Locate and identify every blood parasite.
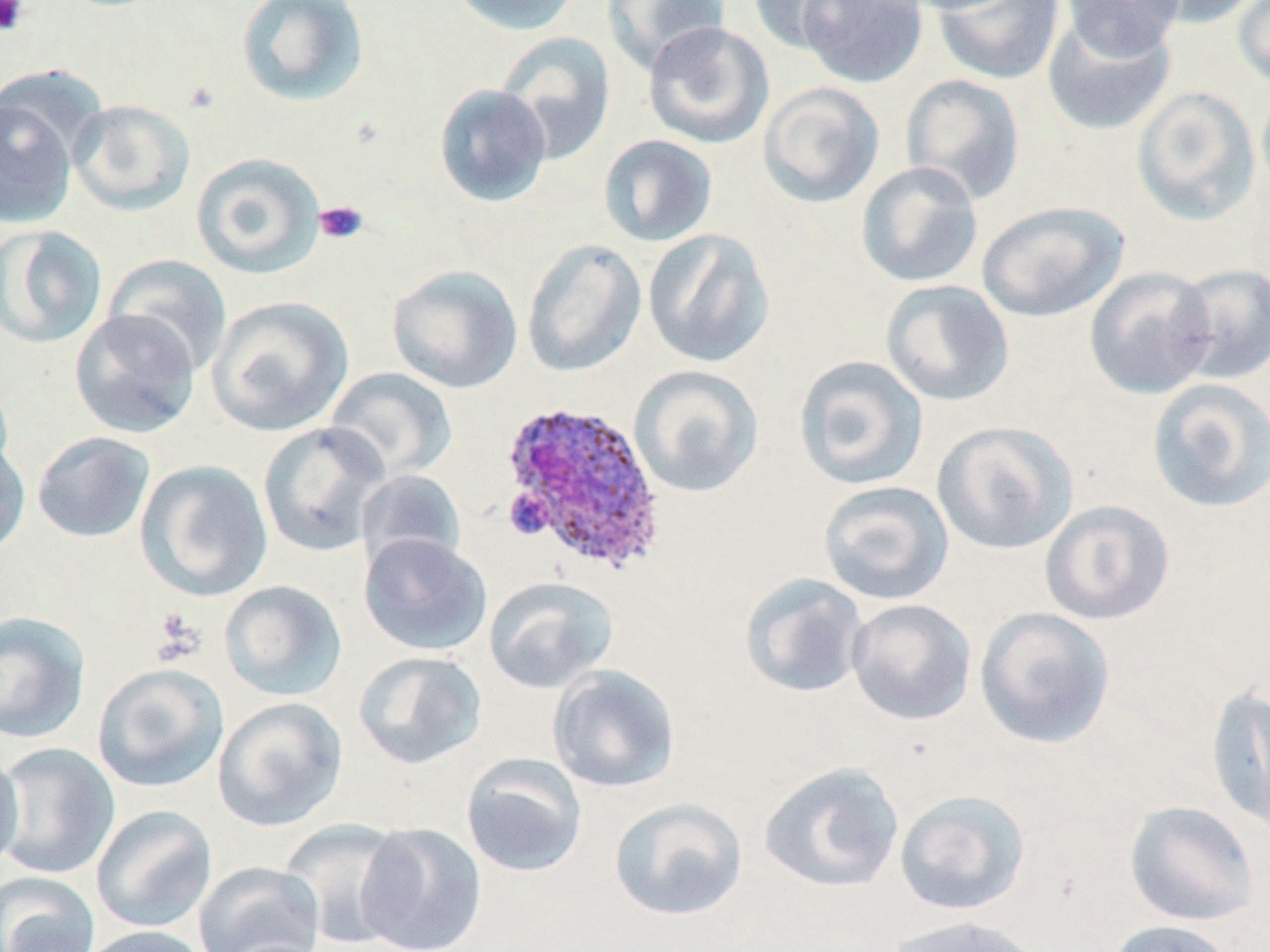

Approximate bounding boxes as named x1/y1/x2/y2 corners in pixels.
Plasmodium ovale-infected red blood cells: (x1=498, y1=398, x2=668, y2=575).
No Plasmodium falciparum, Plasmodium malariae, Plasmodium vivax, Babesia divergens, or Trypanosoma brucei observed.

Summary:
  - Uninfected red blood cell locations: (x1=235, y1=0, x2=370, y2=108), (x1=446, y1=0, x2=583, y2=35), (x1=600, y1=0, x2=731, y2=76), (x1=746, y1=0, x2=868, y2=55), (x1=798, y1=0, x2=929, y2=88), (x1=1062, y1=0, x2=1185, y2=59), (x1=1135, y1=0, x2=1263, y2=29), (x1=1232, y1=0, x2=1270, y2=94), (x1=933, y1=1, x2=1065, y2=85), (x1=1041, y1=9, x2=1176, y2=136), (x1=642, y1=21, x2=775, y2=150), (x1=495, y1=31, x2=616, y2=165), (x1=900, y1=74, x2=1025, y2=205), (x1=757, y1=82, x2=885, y2=208), (x1=1256, y1=83, x2=1270, y2=203), (x1=433, y1=84, x2=553, y2=207), (x1=1131, y1=86, x2=1260, y2=226), (x1=0, y1=91, x2=80, y2=230), (x1=67, y1=99, x2=196, y2=216), (x1=597, y1=134, x2=718, y2=248), (x1=190, y1=152, x2=326, y2=279), (x1=855, y1=161, x2=984, y2=287), (x1=976, y1=200, x2=1128, y2=323), (x1=0, y1=225, x2=108, y2=349), (x1=642, y1=228, x2=775, y2=369), (x1=521, y1=237, x2=647, y2=378), (x1=103, y1=254, x2=232, y2=376), (x1=1172, y1=263, x2=1269, y2=384), (x1=387, y1=264, x2=523, y2=394), (x1=1084, y1=266, x2=1217, y2=400), (x1=880, y1=280, x2=1015, y2=407), (x1=206, y1=295, x2=354, y2=437), (x1=68, y1=309, x2=201, y2=439), (x1=793, y1=355, x2=929, y2=490), (x1=629, y1=365, x2=764, y2=498), (x1=324, y1=367, x2=457, y2=482), (x1=1146, y1=378, x2=1270, y2=513), (x1=932, y1=420, x2=1079, y2=555), (x1=257, y1=421, x2=391, y2=558), (x1=32, y1=431, x2=156, y2=542), (x1=0, y1=436, x2=31, y2=561), (x1=134, y1=459, x2=274, y2=602), (x1=356, y1=469, x2=466, y2=574), (x1=817, y1=480, x2=954, y2=605), (x1=1039, y1=499, x2=1175, y2=625), (x1=358, y1=533, x2=493, y2=656), (x1=739, y1=573, x2=870, y2=699), (x1=483, y1=576, x2=618, y2=694), (x1=219, y1=580, x2=347, y2=702), (x1=846, y1=598, x2=977, y2=726), (x1=974, y1=606, x2=1117, y2=750), (x1=0, y1=611, x2=91, y2=744), (x1=353, y1=650, x2=487, y2=770), (x1=92, y1=662, x2=229, y2=793), (x1=547, y1=664, x2=682, y2=794), (x1=1205, y1=682, x2=1270, y2=830), (x1=212, y1=697, x2=348, y2=832), (x1=0, y1=742, x2=120, y2=880), (x1=0, y1=746, x2=25, y2=874), (x1=461, y1=754, x2=588, y2=878), (x1=758, y1=760, x2=905, y2=893), (x1=894, y1=789, x2=1031, y2=916), (x1=608, y1=797, x2=748, y2=921), (x1=1125, y1=799, x2=1260, y2=927), (x1=90, y1=804, x2=218, y2=934), (x1=279, y1=818, x2=412, y2=950), (x1=355, y1=822, x2=487, y2=952), (x1=193, y1=861, x2=325, y2=952), (x1=1, y1=872, x2=100, y2=952), (x1=884, y1=915, x2=1044, y2=952), (x1=1106, y1=920, x2=1237, y2=952), (x1=78, y1=925, x2=216, y2=952)
  - Platelet locations: (x1=0, y1=0, x2=29, y2=36), (x1=314, y1=201, x2=369, y2=245), (x1=151, y1=608, x2=207, y2=665)
  - Slide-level diagnosis: Plasmodium ovale
  - Modality: light microscopy
  - Stain: May-Grünwald-Giemsa
  - Image size: 1270×952 pixels
  - Preparation: thin blood smear
  - Field of view: single
  - Magnification: 1000x